Assess this cell for malaria.
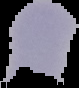
It is uninfected.

image size = 79×88 pixels
image type = cell region segmented out of the field of view; surrounding area masked to black
preparation = thin blood smear